Identify the parasite.
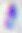

This is Toxoplasma gondii.

Summary:
  - Magnification: 400x
  - Modality: photomicrograph